Look for Plasmodium parasites.
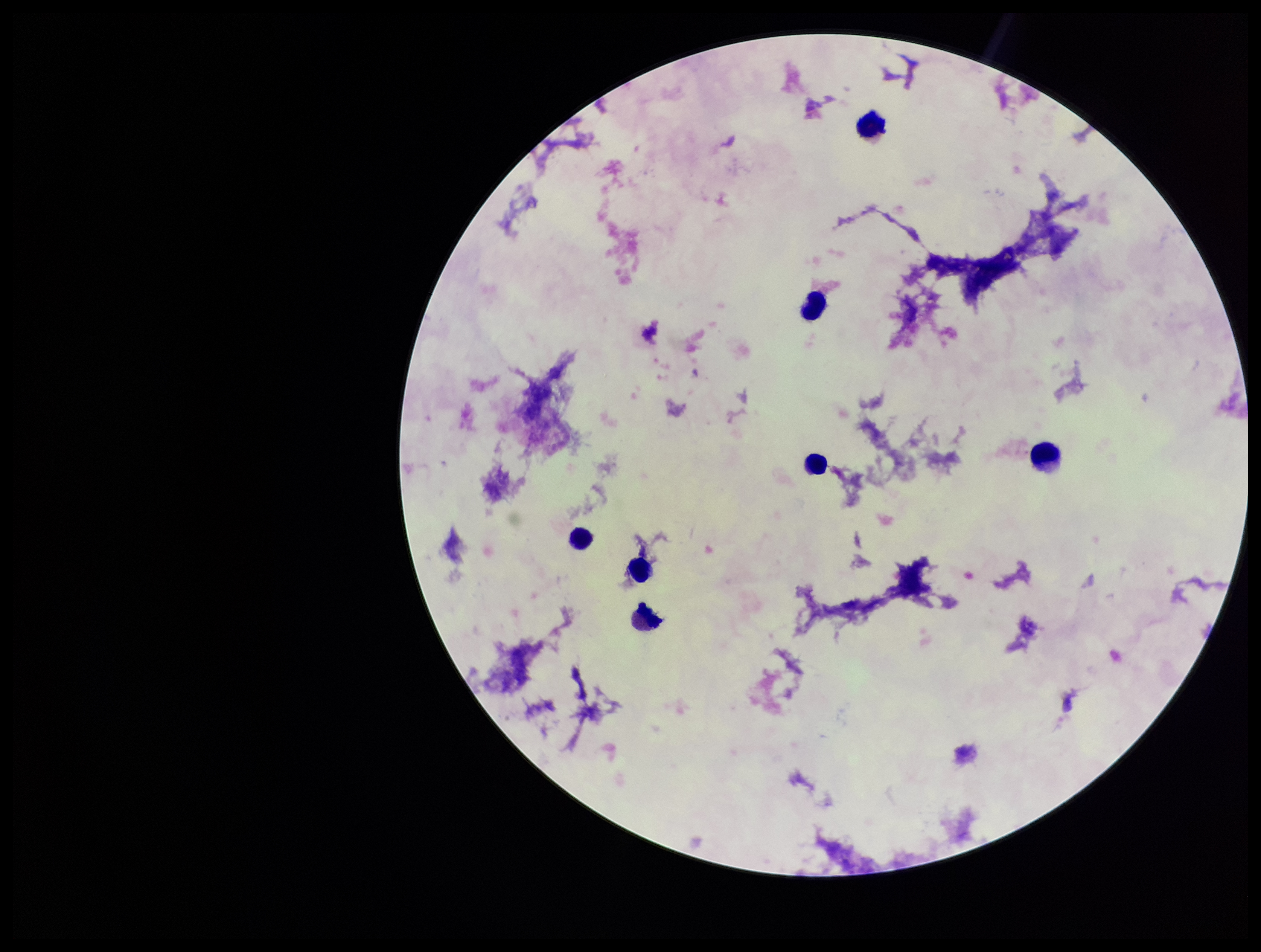

None detected.

leukocyte count = 7
image size = 1261×952 pixels
capture = smartphone photograph through the microscope eyepiece
stain = Giemsa
patient malaria status = negative
preparation = thick smear
field of view = single
parasite count = 0